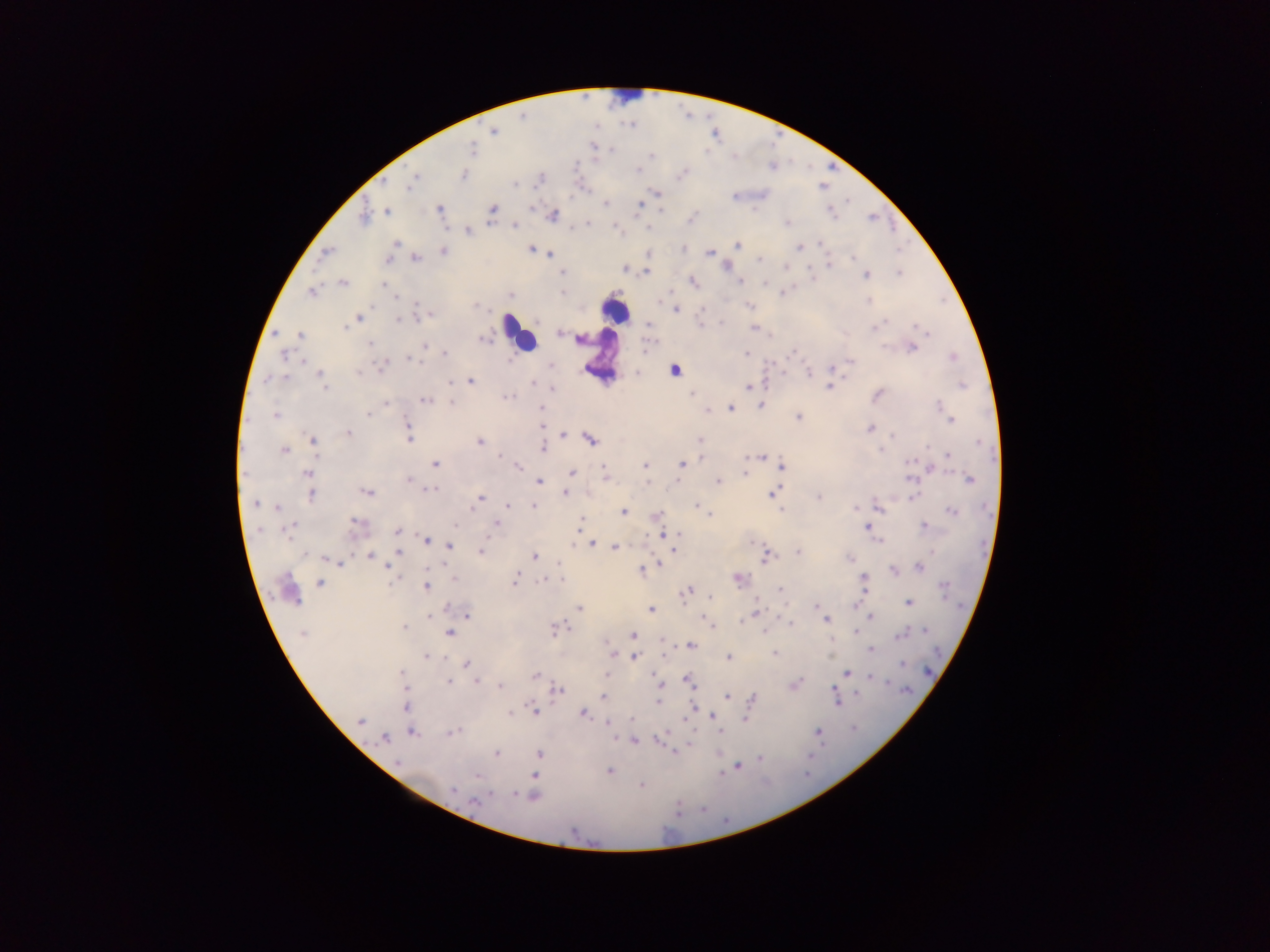 Approximate centers as [x, y] in pixels. Leukocyte locations: [626, 99], [615, 309], [510, 324], [520, 334], [601, 356], [675, 369]. Plasmodium parasite locations: [493, 131], [594, 147], [471, 151], [651, 155], [638, 169], [462, 175], [413, 179], [655, 193], [606, 203], [639, 204], [439, 209], [662, 209], [492, 210], [386, 211], [553, 215], [364, 218], [692, 218], [788, 223], [513, 225], [467, 231], [819, 242], [395, 243], [737, 245], [799, 247], [530, 249], [684, 249], [443, 250], [327, 253], [709, 253], [551, 255], [758, 257], [852, 257], [389, 258], [416, 259], [829, 264], [727, 266], [623, 268], [646, 271], [562, 273], [900, 273], [866, 274], [693, 281], [343, 282], [740, 282], [384, 283], [312, 291], [783, 292], [511, 296], [395, 297], [867, 300], [475, 305], [750, 305], [676, 309], [428, 313], [358, 318], [399, 321], [649, 323], [876, 326], [345, 327], [754, 329], [559, 333], [300, 335], [482, 338], [370, 344], [424, 346], [909, 347], [647, 348], [745, 353], [444, 354], [285, 355], [410, 359], [847, 361], [381, 363], [832, 366], [637, 374], [808, 374], [321, 376], [471, 380], [448, 381], [534, 384], [962, 385], [830, 386], [748, 387], [552, 388], [693, 393], [878, 395], [505, 396], [425, 400], [451, 400], [386, 402], [760, 405], [731, 407], [541, 408], [708, 409], [368, 413], [275, 415], [798, 416], [951, 419], [541, 425], [407, 428], [870, 429], [347, 433], [563, 435], [409, 436], [591, 439], [312, 441], [479, 441], [699, 441], [541, 447], [283, 450], [948, 455], [499, 456], [760, 456], [702, 458], [435, 463], [646, 464], [682, 464], [781, 466], [519, 467], [930, 468], [605, 470], [571, 473], [744, 473], [307, 474], [604, 477], [408, 479], [969, 479], [538, 481], [718, 481], [645, 482], [430, 488], [366, 491], [565, 492], [773, 493], [311, 494], [819, 496], [480, 497], [255, 503], [507, 505], [534, 505], [696, 505], [277, 507], [878, 508], [783, 510], [624, 511], [952, 511], [709, 513], [656, 515], [496, 523], [580, 523], [357, 524], [456, 526], [924, 526], [867, 527], [287, 529], [398, 531], [664, 532], [678, 535], [427, 540], [592, 544], [450, 545], [615, 547], [674, 547], [480, 551], [797, 551], [399, 553], [369, 555], [766, 555], [535, 556], [850, 558], [326, 559], [335, 562], [659, 565], [387, 566], [919, 566], [639, 570], [892, 571], [515, 578], [737, 578], [542, 581], [863, 581], [320, 583], [425, 585], [287, 589], [687, 590], [780, 590], [711, 598], [757, 602], [908, 603], [816, 606], [579, 607], [651, 609], [756, 612], [431, 615], [466, 615], [870, 616], [826, 619], [741, 620], [789, 621], [709, 625], [404, 627], [554, 629], [855, 631], [924, 631], [763, 632], [448, 633], [303, 634], [900, 635], [633, 636], [689, 645], [870, 649], [663, 654], [774, 654], [426, 655], [613, 655], [728, 656], [634, 657], [901, 663], [466, 664], [402, 672], [846, 673], [535, 675], [607, 675], [870, 677], [688, 679], [448, 680], [476, 680], [793, 684], [500, 686], [662, 687], [556, 690], [727, 696], [603, 697], [835, 698], [752, 700], [658, 701], [406, 706], [692, 707], [533, 709], [509, 712], [582, 712], [711, 716], [744, 718], [361, 721], [607, 723], [818, 731], [412, 732], [452, 732], [385, 737], [659, 738], [633, 740], [675, 750], [496, 753], [718, 753], [538, 754], [759, 758], [737, 766], [608, 771], [719, 773], [534, 775], [641, 784], [452, 790], [533, 796], [475, 801]. Photographed through a microscope with a mobile-phone camera. One field of view. Image is 1270×952 pixels. Thick blood film. Collected in Ghana.